Assess the morphology of the red blood cells.
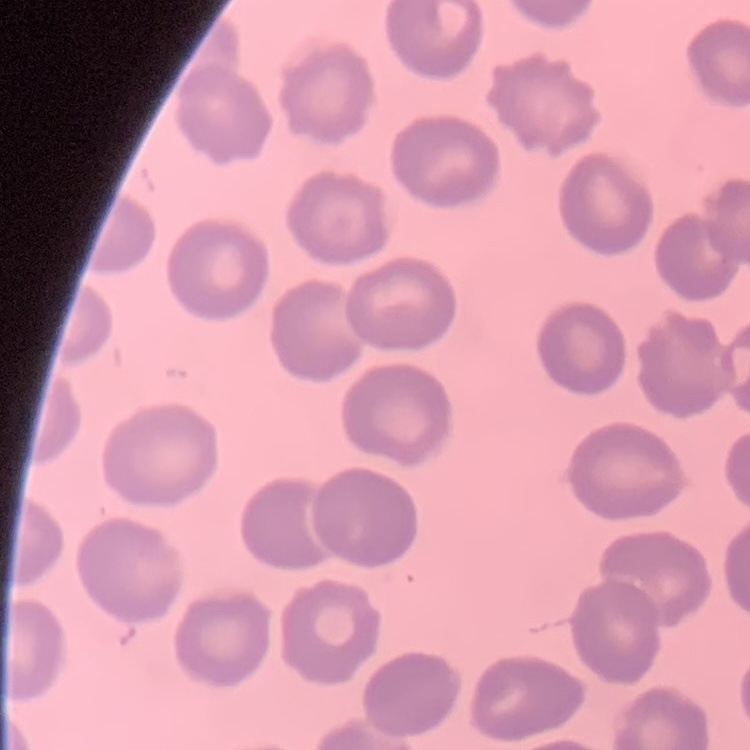

They show no rouleaux formation.

Summary:
  - Image type: square crop of a larger photomicrograph
  - Preparation: thin blood film
  - Stain: Field's or Giemsa